State which parasite is depicted.
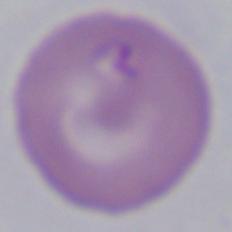

This is Babesia.

Photomicrograph. Captured at 1000x magnification.